Comment on the morphology of the red blood cells.
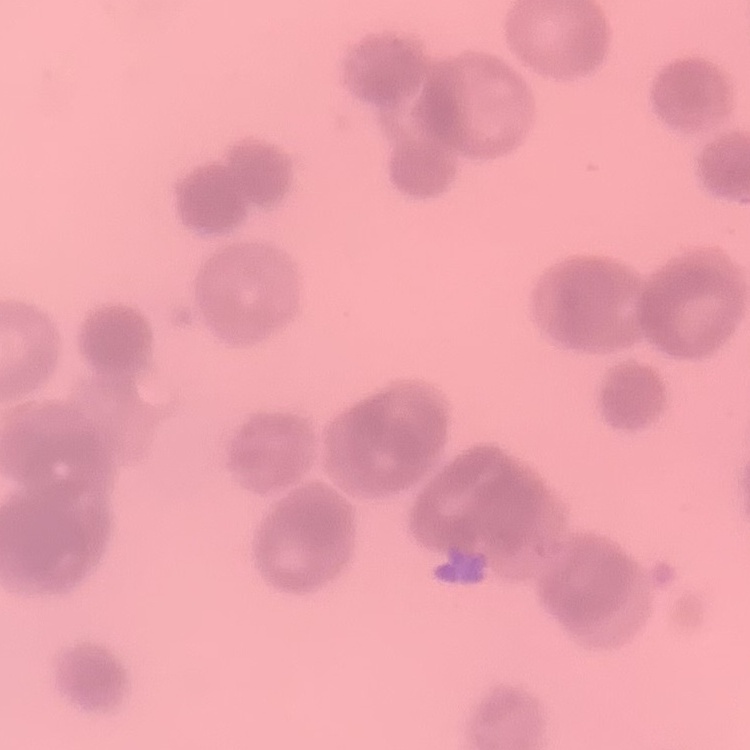

They show rouleaux formation.

{
  "preparation": "thin peripheral smear",
  "image_type": "square crop of a larger photomicrograph",
  "stain": "Field's or Giemsa"
}